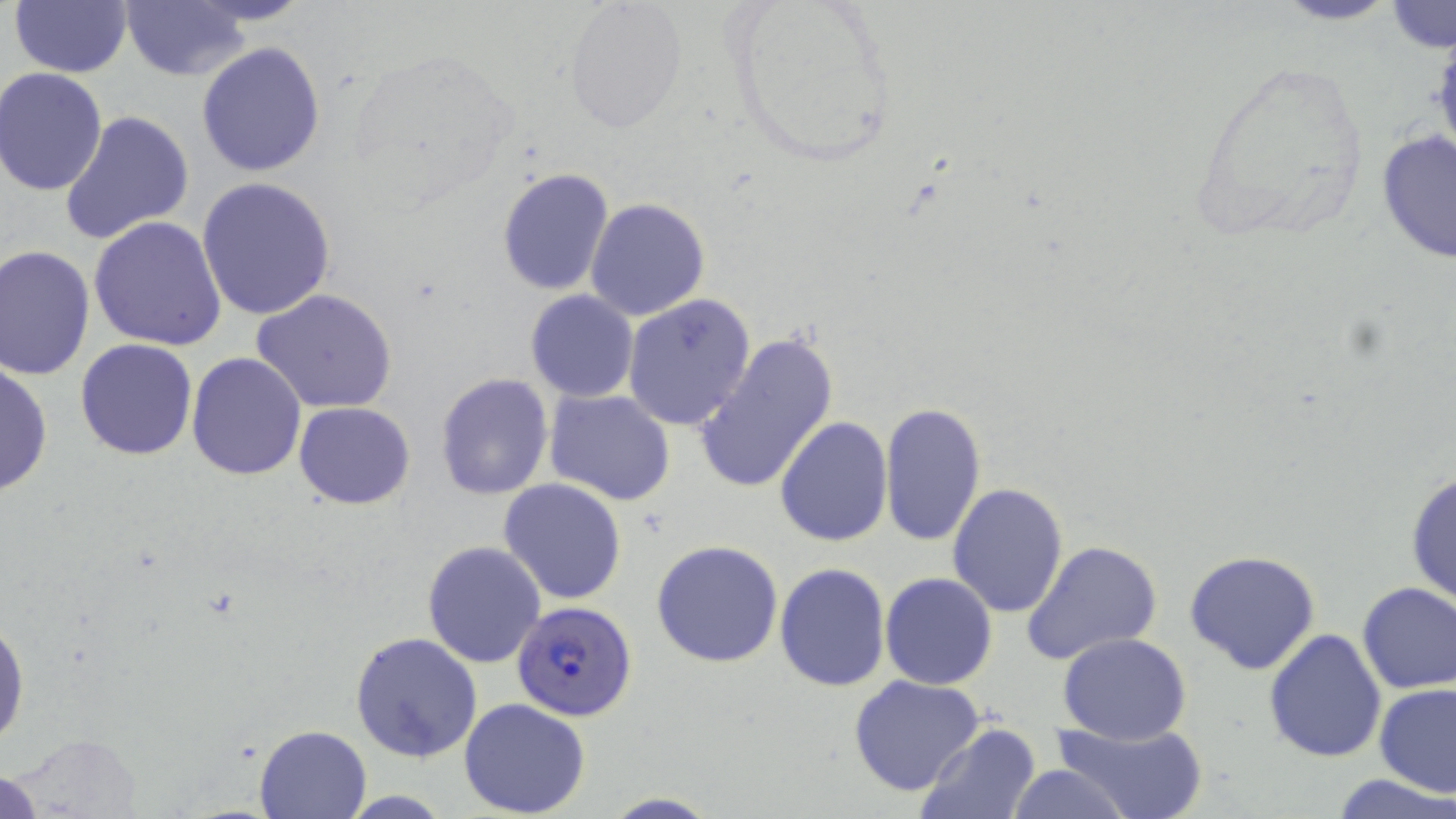
slide-level diagnosis = Plasmodium falciparum
image size = 1456×819 pixels
modality = optical microscopy
Plasmodium falciparum-infected red blood cell locations = approximate bounding boxes as [x1, y1, x2, y2] in pixels: [511, 598, 637, 720]
uninfected red blood cell locations = approximate bounding boxes as [x1, y1, x2, y2] in pixels: [8, 0, 133, 78], [118, 0, 257, 82], [1269, 0, 1403, 26], [565, 1, 687, 133], [1386, 2, 1454, 52], [196, 40, 328, 179], [1, 67, 111, 196], [59, 109, 194, 249], [1376, 129, 1456, 265], [497, 167, 615, 296], [195, 178, 338, 323], [585, 196, 710, 321], [88, 217, 229, 354], [1, 244, 96, 380], [253, 289, 399, 415], [525, 291, 638, 403], [623, 293, 757, 432], [693, 330, 840, 496], [74, 338, 198, 460], [185, 352, 306, 481], [0, 359, 53, 498], [434, 371, 555, 501], [544, 389, 676, 507], [293, 401, 415, 509], [879, 401, 988, 548], [773, 415, 893, 546], [1405, 469, 1455, 608], [499, 479, 627, 605], [948, 483, 1069, 618], [1022, 539, 1164, 669], [651, 540, 783, 668], [421, 541, 546, 667], [1184, 550, 1322, 675], [774, 562, 890, 691], [880, 572, 998, 691], [1356, 581, 1456, 692], [0, 613, 28, 752], [1263, 628, 1386, 761], [350, 630, 484, 761], [1058, 632, 1192, 743], [848, 674, 985, 796], [1375, 684, 1456, 799], [459, 698, 591, 817], [1050, 715, 1208, 819], [914, 722, 1042, 819], [255, 725, 370, 817], [1002, 763, 1133, 818], [0, 768, 46, 817], [1336, 774, 1452, 818], [598, 793, 722, 818]
stain = May-Grünwald-Giemsa
preparation = thin blood smear
field of view = single
magnification = 1000x